Give the extent of all uninfected red blood cells.
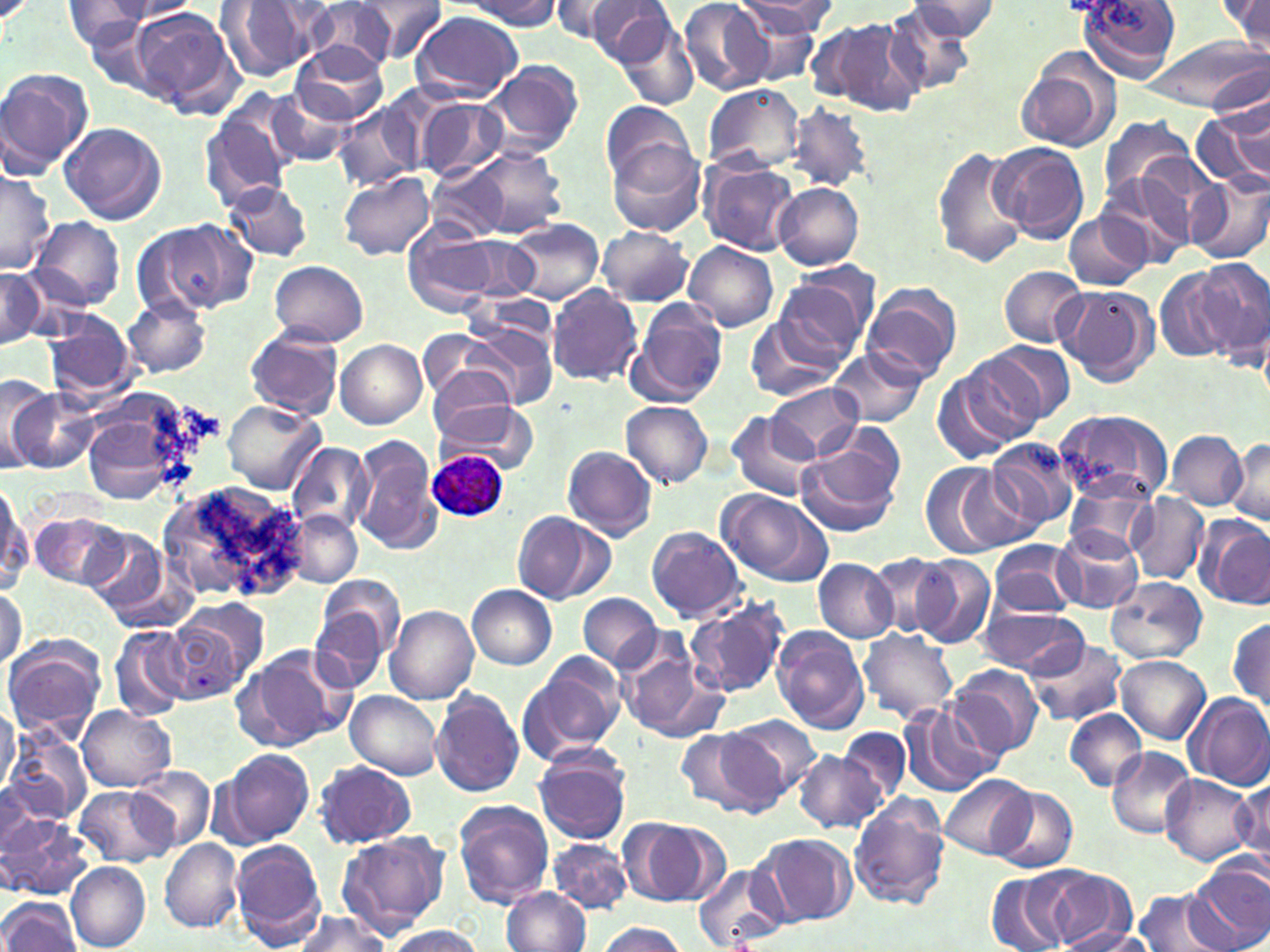

Approximate bounding boxes as named x1/y1/x2/y2 corners in pixels.
Uninfected red blood cells: (x1=355, y1=0, x2=447, y2=62), (x1=462, y1=0, x2=563, y2=29), (x1=548, y1=0, x2=638, y2=43), (x1=679, y1=0, x2=771, y2=95), (x1=723, y1=0, x2=829, y2=72), (x1=733, y1=0, x2=835, y2=38), (x1=1079, y1=0, x2=1179, y2=80), (x1=98, y1=1, x2=201, y2=23), (x1=216, y1=1, x2=322, y2=81), (x1=305, y1=1, x2=404, y2=71), (x1=581, y1=1, x2=677, y2=67), (x1=905, y1=1, x2=1002, y2=40), (x1=1219, y1=1, x2=1270, y2=50), (x1=62, y1=2, x2=154, y2=51), (x1=884, y1=4, x2=977, y2=96), (x1=128, y1=6, x2=237, y2=111), (x1=410, y1=11, x2=522, y2=101), (x1=613, y1=12, x2=701, y2=110), (x1=810, y1=18, x2=923, y2=116), (x1=85, y1=19, x2=160, y2=88), (x1=1143, y1=37, x2=1270, y2=115), (x1=290, y1=42, x2=386, y2=124), (x1=1017, y1=50, x2=1122, y2=156), (x1=482, y1=62, x2=584, y2=159), (x1=0, y1=67, x2=92, y2=174), (x1=702, y1=82, x2=805, y2=174), (x1=265, y1=90, x2=355, y2=169), (x1=413, y1=95, x2=510, y2=182), (x1=202, y1=97, x2=297, y2=208), (x1=599, y1=99, x2=697, y2=191), (x1=333, y1=104, x2=420, y2=193), (x1=788, y1=104, x2=873, y2=192), (x1=1193, y1=112, x2=1268, y2=186), (x1=1098, y1=115, x2=1195, y2=208), (x1=59, y1=122, x2=167, y2=226), (x1=609, y1=141, x2=707, y2=237), (x1=989, y1=143, x2=1088, y2=242), (x1=934, y1=145, x2=1027, y2=268), (x1=451, y1=146, x2=567, y2=240), (x1=1135, y1=156, x2=1228, y2=245), (x1=699, y1=159, x2=799, y2=256), (x1=427, y1=161, x2=510, y2=239), (x1=0, y1=168, x2=55, y2=275), (x1=337, y1=172, x2=436, y2=260), (x1=1187, y1=173, x2=1270, y2=264), (x1=1098, y1=174, x2=1195, y2=267), (x1=224, y1=181, x2=313, y2=263), (x1=773, y1=181, x2=865, y2=270), (x1=1062, y1=212, x2=1151, y2=292), (x1=31, y1=216, x2=124, y2=310), (x1=140, y1=217, x2=256, y2=318), (x1=505, y1=218, x2=601, y2=305), (x1=404, y1=222, x2=498, y2=316), (x1=597, y1=226, x2=695, y2=305), (x1=464, y1=237, x2=538, y2=299), (x1=683, y1=242, x2=780, y2=330), (x1=1192, y1=258, x2=1270, y2=360), (x1=269, y1=260, x2=368, y2=348), (x1=999, y1=266, x2=1086, y2=348), (x1=0, y1=267, x2=46, y2=350), (x1=1155, y1=269, x2=1242, y2=365), (x1=772, y1=277, x2=868, y2=371), (x1=860, y1=283, x2=961, y2=383), (x1=546, y1=284, x2=642, y2=386), (x1=1054, y1=284, x2=1159, y2=388), (x1=125, y1=296, x2=213, y2=378), (x1=626, y1=302, x2=727, y2=406), (x1=46, y1=313, x2=136, y2=397), (x1=745, y1=314, x2=846, y2=401), (x1=462, y1=318, x2=560, y2=410), (x1=246, y1=326, x2=346, y2=419), (x1=421, y1=331, x2=515, y2=408), (x1=335, y1=340, x2=428, y2=429), (x1=990, y1=342, x2=1077, y2=424), (x1=828, y1=348, x2=925, y2=427), (x1=957, y1=348, x2=1056, y2=445), (x1=429, y1=365, x2=516, y2=437), (x1=933, y1=366, x2=1028, y2=464), (x1=1, y1=374, x2=55, y2=473), (x1=769, y1=383, x2=862, y2=462), (x1=9, y1=391, x2=94, y2=473), (x1=435, y1=395, x2=539, y2=473), (x1=80, y1=399, x2=194, y2=509), (x1=224, y1=400, x2=323, y2=493), (x1=620, y1=400, x2=715, y2=488), (x1=1053, y1=408, x2=1175, y2=505), (x1=726, y1=412, x2=818, y2=500), (x1=1165, y1=431, x2=1248, y2=510), (x1=795, y1=434, x2=904, y2=538), (x1=353, y1=437, x2=442, y2=554), (x1=984, y1=438, x2=1079, y2=536), (x1=1227, y1=438, x2=1270, y2=528), (x1=287, y1=441, x2=375, y2=535), (x1=563, y1=445, x2=658, y2=540), (x1=919, y1=460, x2=1023, y2=559), (x1=158, y1=479, x2=311, y2=605), (x1=0, y1=483, x2=31, y2=597), (x1=1065, y1=483, x2=1156, y2=560), (x1=714, y1=489, x2=829, y2=586), (x1=1126, y1=493, x2=1209, y2=583), (x1=287, y1=510, x2=362, y2=589), (x1=30, y1=511, x2=127, y2=591), (x1=511, y1=511, x2=612, y2=606), (x1=1194, y1=515, x2=1270, y2=609), (x1=85, y1=524, x2=170, y2=617), (x1=645, y1=525, x2=747, y2=622), (x1=1051, y1=529, x2=1143, y2=613), (x1=987, y1=541, x2=1079, y2=618), (x1=868, y1=553, x2=951, y2=638), (x1=912, y1=555, x2=995, y2=648), (x1=813, y1=558, x2=896, y2=643), (x1=313, y1=573, x2=405, y2=670), (x1=1106, y1=577, x2=1208, y2=664), (x1=0, y1=584, x2=26, y2=670), (x1=467, y1=584, x2=558, y2=670), (x1=579, y1=594, x2=663, y2=672), (x1=686, y1=595, x2=790, y2=699), (x1=978, y1=605, x2=1087, y2=677), (x1=385, y1=606, x2=480, y2=704), (x1=162, y1=607, x2=258, y2=703), (x1=308, y1=607, x2=392, y2=695), (x1=1229, y1=616, x2=1269, y2=712), (x1=108, y1=625, x2=188, y2=721), (x1=772, y1=628, x2=869, y2=734), (x1=857, y1=629, x2=959, y2=723), (x1=2, y1=636, x2=107, y2=741), (x1=1026, y1=638, x2=1127, y2=726), (x1=616, y1=640, x2=727, y2=744), (x1=241, y1=645, x2=354, y2=749), (x1=517, y1=654, x2=628, y2=765), (x1=1116, y1=655, x2=1210, y2=744), (x1=946, y1=664, x2=1043, y2=762), (x1=431, y1=687, x2=524, y2=797), (x1=344, y1=691, x2=443, y2=780), (x1=1186, y1=692, x2=1270, y2=789), (x1=0, y1=701, x2=20, y2=799), (x1=78, y1=705, x2=175, y2=791), (x1=898, y1=705, x2=996, y2=797), (x1=1065, y1=710, x2=1147, y2=791), (x1=727, y1=715, x2=822, y2=801), (x1=839, y1=726, x2=910, y2=805), (x1=688, y1=729, x2=786, y2=816), (x1=5, y1=731, x2=91, y2=828), (x1=1106, y1=747, x2=1196, y2=838), (x1=214, y1=748, x2=314, y2=849), (x1=533, y1=749, x2=632, y2=845), (x1=793, y1=751, x2=886, y2=834), (x1=310, y1=763, x2=418, y2=848), (x1=130, y1=765, x2=215, y2=851), (x1=1161, y1=774, x2=1257, y2=867), (x1=938, y1=775, x2=1035, y2=859), (x1=1233, y1=777, x2=1269, y2=874), (x1=73, y1=786, x2=178, y2=866), (x1=990, y1=787, x2=1078, y2=874), (x1=848, y1=792, x2=950, y2=910), (x1=452, y1=799, x2=554, y2=910), (x1=1, y1=813, x2=93, y2=899), (x1=618, y1=818, x2=722, y2=908), (x1=337, y1=830, x2=449, y2=937), (x1=756, y1=833, x2=856, y2=925), (x1=159, y1=838, x2=243, y2=933), (x1=547, y1=838, x2=632, y2=913), (x1=231, y1=840, x2=325, y2=946), (x1=1189, y1=860, x2=1270, y2=952), (x1=67, y1=863, x2=150, y2=950), (x1=693, y1=863, x2=789, y2=950), (x1=1035, y1=870, x2=1135, y2=952), (x1=986, y1=871, x2=1068, y2=952), (x1=502, y1=887, x2=590, y2=952), (x1=1133, y1=888, x2=1230, y2=952), (x1=0, y1=897, x2=80, y2=951), (x1=289, y1=910, x2=390, y2=951), (x1=597, y1=923, x2=688, y2=952), (x1=385, y1=926, x2=486, y2=952), (x1=1054, y1=927, x2=1157, y2=952).

Summary:
  - Plasmodium ovale-infected red blood cell locations: (x1=427, y1=449, x2=507, y2=520)
  - Slide-level diagnosis: Plasmodium ovale
  - Stain: May-Grünwald-Giemsa
  - Preparation: thin blood smear
  - Field of view: single
  - Magnification: 1000x
  - Image size: 1270×952 pixels
  - Modality: optical microscopy